Report the malaria status of this cell.
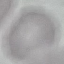

Uninfected.

Giemsa stain. Automatically extracted cell patch, resized to 64 × 64 pixels. Acquired by smartphone through the microscope eyepiece. Thin smear of blood.